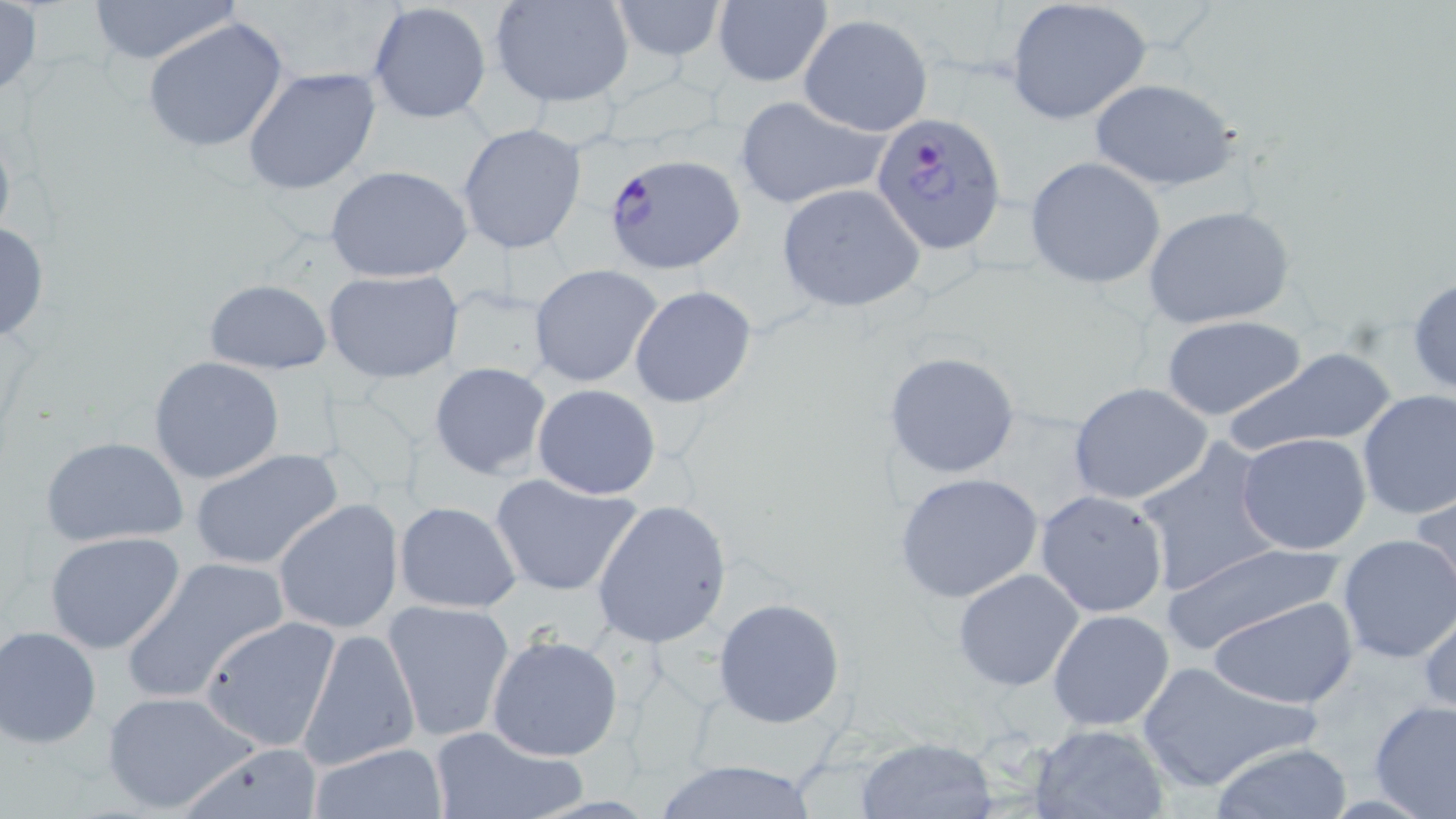
slide_level_diagnosis: Plasmodium falciparum
magnification: 1000x
modality: optical microscopy
preparation: thin blood smear
image_size: 1456×819 pixels
plasmodium_falciparum_infected_red_blood_cell_locations: 'approximate bounding boxes as named x1/y1/x2/y2 corners in pixels: (x1=870, y1=112, x2=1007, y2=255), (x1=603, y1=154, x2=748, y2=275)'
field_of_view: one of a larger specimen
uninfected_red_blood_cell_locations: 'approximate bounding boxes as named x1/y1/x2/y2 corners in pixels: (x1=83, y1=0, x2=241, y2=67), (x1=491, y1=0, x2=635, y2=108), (x1=608, y1=0, x2=728, y2=60), (x1=1006, y1=0, x2=1153, y2=125), (x1=368, y1=1, x2=493, y2=122), (x1=713, y1=1, x2=833, y2=88), (x1=0, y1=2, x2=45, y2=101), (x1=796, y1=13, x2=933, y2=137), (x1=141, y1=16, x2=292, y2=156), (x1=243, y1=66, x2=381, y2=197), (x1=1088, y1=78, x2=1242, y2=193), (x1=733, y1=94, x2=891, y2=210), (x1=456, y1=124, x2=588, y2=255), (x1=1025, y1=156, x2=1166, y2=289), (x1=324, y1=163, x2=474, y2=283), (x1=776, y1=184, x2=925, y2=312), (x1=1143, y1=204, x2=1296, y2=329), (x1=0, y1=221, x2=51, y2=344), (x1=530, y1=264, x2=663, y2=388), (x1=322, y1=269, x2=464, y2=383), (x1=1408, y1=275, x2=1456, y2=400), (x1=203, y1=278, x2=332, y2=375), (x1=440, y1=285, x2=557, y2=392), (x1=630, y1=285, x2=758, y2=409), (x1=1159, y1=315, x2=1308, y2=422), (x1=1225, y1=347, x2=1399, y2=456), (x1=883, y1=349, x2=1021, y2=480), (x1=148, y1=356, x2=286, y2=485), (x1=429, y1=362, x2=552, y2=480), (x1=1067, y1=382, x2=1213, y2=506), (x1=532, y1=383, x2=661, y2=499), (x1=1356, y1=390, x2=1456, y2=523), (x1=1237, y1=433, x2=1372, y2=556), (x1=38, y1=434, x2=191, y2=548), (x1=1130, y1=439, x2=1285, y2=600), (x1=189, y1=449, x2=345, y2=572), (x1=894, y1=472, x2=1043, y2=603), (x1=490, y1=475, x2=643, y2=598), (x1=1411, y1=486, x2=1456, y2=612), (x1=1034, y1=490, x2=1169, y2=617), (x1=272, y1=498, x2=404, y2=633), (x1=590, y1=499, x2=732, y2=649), (x1=393, y1=500, x2=522, y2=613), (x1=43, y1=531, x2=189, y2=655), (x1=1335, y1=533, x2=1456, y2=664), (x1=1159, y1=540, x2=1348, y2=654), (x1=121, y1=555, x2=291, y2=704), (x1=953, y1=567, x2=1084, y2=694), (x1=1210, y1=596, x2=1359, y2=709), (x1=713, y1=598, x2=846, y2=728), (x1=1418, y1=598, x2=1455, y2=718), (x1=382, y1=599, x2=514, y2=741), (x1=1048, y1=608, x2=1176, y2=731), (x1=200, y1=615, x2=344, y2=763), (x1=1, y1=625, x2=103, y2=748), (x1=298, y1=627, x2=420, y2=771), (x1=486, y1=633, x2=623, y2=761), (x1=1133, y1=661, x2=1316, y2=794), (x1=100, y1=689, x2=260, y2=816), (x1=1368, y1=700, x2=1456, y2=819), (x1=426, y1=722, x2=584, y2=819), (x1=1028, y1=722, x2=1173, y2=818), (x1=855, y1=736, x2=997, y2=817), (x1=1212, y1=740, x2=1351, y2=818), (x1=174, y1=741, x2=328, y2=819), (x1=308, y1=742, x2=448, y2=819), (x1=652, y1=759, x2=822, y2=818)'
stain: May-Grünwald-Giemsa